Describe the morphology of the red blood cells.
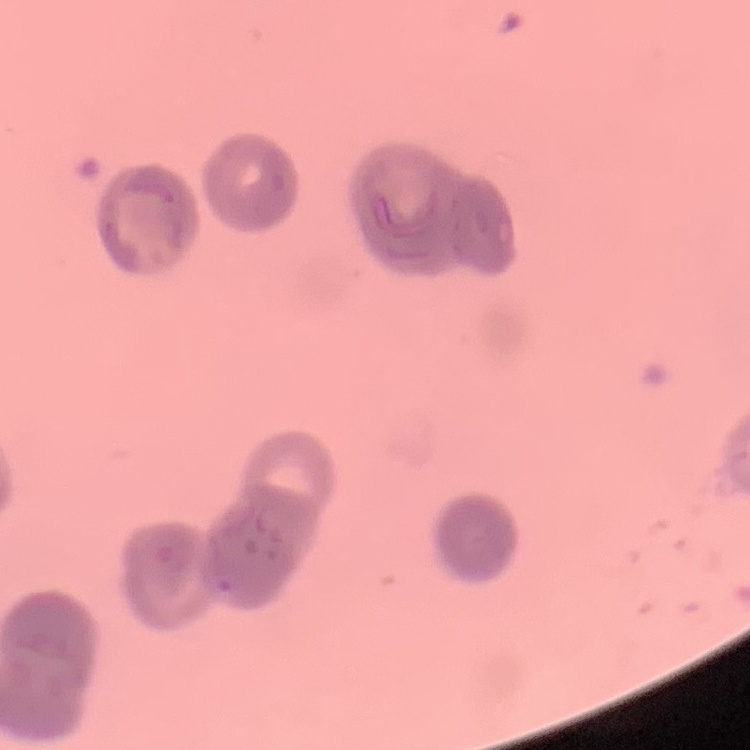

They show rouleaux formation.

image_type: square crop of a larger photomicrograph
preparation: thin blood film
stain: Field's or Giemsa